Report the malaria status of this cell.
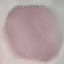

It is uninfected.

Summary:
  - Image type: cell patch, automatically extracted from a larger field of view and resized to 64 × 64 pixels
  - Capture: smartphone camera at the microscope eyepiece
  - Preparation: thin blood film
  - Stain: Giemsa